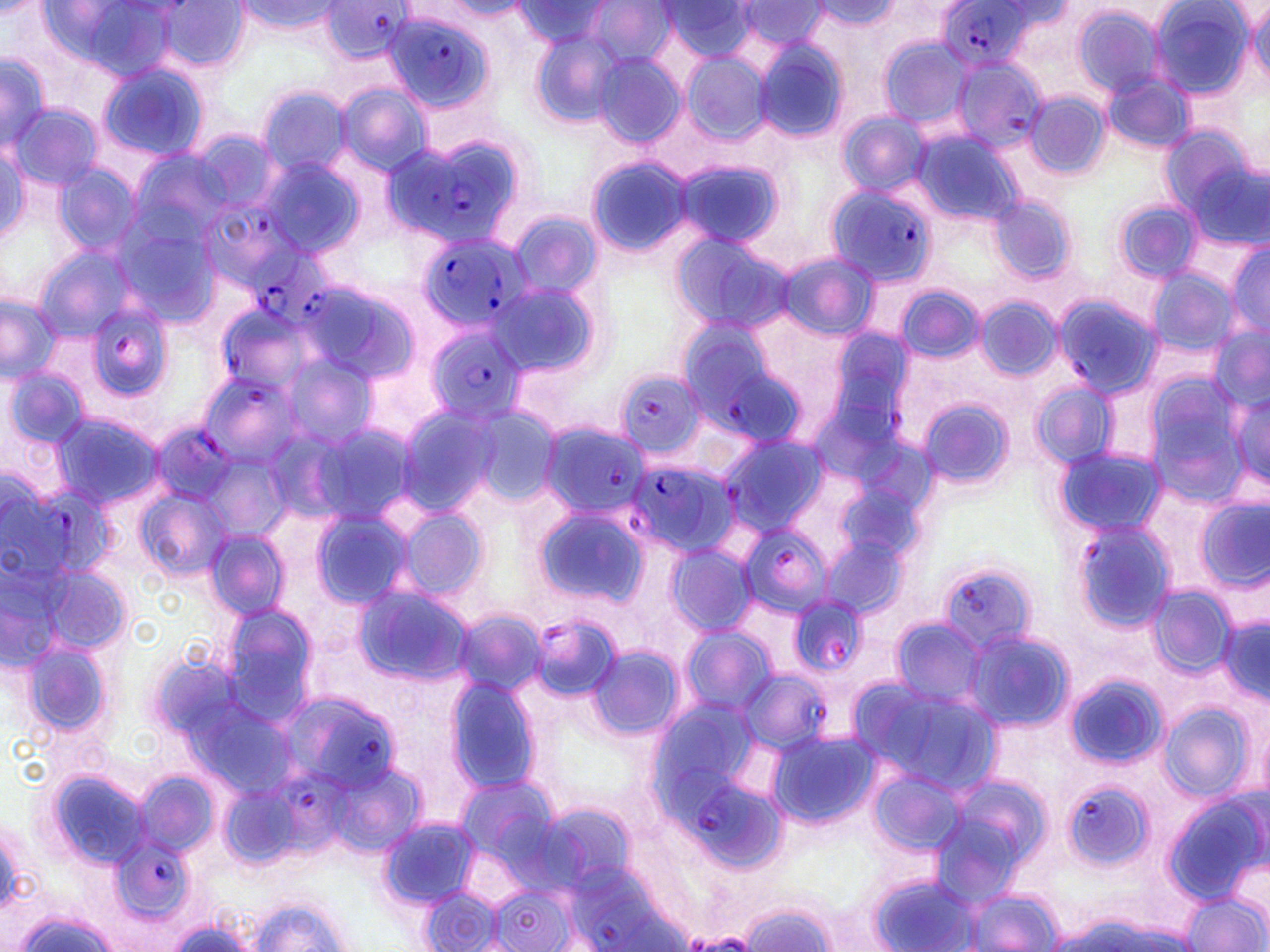
slide-level diagnosis = Plasmodium falciparum
stain = May-Grünwald-Giemsa
modality = optical microscopy
Plasmodium falciparum-infected red blood cell locations = approximate bounding boxes as (x1, y1, x2, y2) in pixels: (933, 1, 1053, 72), (377, 5, 498, 117), (948, 56, 1051, 154), (386, 130, 528, 249), (824, 182, 940, 287), (202, 204, 304, 291), (416, 229, 531, 336), (249, 242, 335, 324), (1052, 293, 1162, 399), (86, 298, 178, 403), (213, 301, 318, 398), (674, 313, 807, 445), (422, 322, 529, 426), (196, 369, 307, 469), (611, 369, 707, 459), (151, 422, 241, 503), (538, 422, 647, 519), (718, 436, 827, 535), (627, 458, 737, 561), (11, 477, 120, 585), (1072, 518, 1178, 634), (738, 523, 830, 620), (940, 565, 1041, 656), (787, 596, 869, 679), (739, 669, 830, 752), (287, 699, 398, 796), (669, 762, 754, 851), (267, 775, 361, 860), (1061, 779, 1153, 873), (108, 832, 194, 932)
image size = 1270×952 pixels
magnification = 1000x
field of view = one of a larger specimen
preparation = thin blood smear
uninfected red blood cell locations = approximate bounding boxes as (x1, y1, x2, y2) in pixels: (0, 0, 49, 17), (153, 1, 249, 74), (236, 1, 344, 37), (512, 1, 618, 48), (664, 1, 757, 62), (809, 1, 904, 33), (1147, 1, 1256, 100), (42, 2, 181, 82), (444, 2, 529, 19), (583, 2, 676, 66), (735, 2, 835, 51), (1246, 4, 1270, 82), (1070, 6, 1170, 98), (528, 30, 625, 129), (877, 37, 973, 129), (752, 38, 850, 144), (592, 51, 687, 146), (680, 52, 771, 146), (0, 56, 52, 150), (96, 62, 210, 163), (1103, 74, 1195, 154), (335, 82, 433, 175), (256, 86, 353, 177), (1024, 91, 1112, 180), (9, 104, 101, 192), (836, 111, 930, 198), (909, 125, 1023, 232), (0, 137, 30, 247), (1177, 141, 1267, 250), (128, 148, 231, 244), (257, 155, 369, 261), (586, 156, 696, 257), (672, 158, 786, 252), (52, 162, 145, 259), (989, 195, 1077, 285), (1113, 198, 1201, 284), (509, 211, 603, 302), (111, 213, 226, 331), (667, 230, 795, 332), (1226, 242, 1269, 340), (32, 245, 142, 343), (776, 252, 878, 340), (1145, 267, 1237, 357), (487, 276, 607, 383), (301, 278, 421, 390), (893, 283, 986, 365), (0, 292, 63, 383), (974, 296, 1062, 383), (1209, 324, 1270, 416), (271, 351, 379, 455), (4, 365, 90, 453), (1139, 373, 1254, 500), (1031, 382, 1118, 471), (1227, 388, 1269, 489), (917, 396, 1014, 492), (395, 402, 531, 519), (49, 411, 164, 512), (309, 419, 420, 528), (1056, 445, 1167, 538), (203, 454, 290, 539), (137, 486, 231, 583), (1194, 499, 1269, 591), (306, 504, 420, 612), (388, 504, 491, 605), (534, 504, 651, 612), (204, 529, 290, 622), (821, 536, 906, 619), (663, 542, 758, 639), (0, 549, 81, 675), (32, 560, 132, 662), (354, 584, 477, 688), (1147, 584, 1237, 679), (219, 602, 319, 719), (453, 608, 548, 701), (527, 610, 624, 705), (1216, 615, 1270, 699), (887, 618, 992, 712), (958, 625, 1074, 732), (679, 628, 777, 716), (15, 633, 120, 744), (585, 644, 684, 742), (1064, 672, 1170, 771), (444, 675, 542, 794), (853, 677, 1001, 800), (1158, 703, 1255, 802), (766, 729, 879, 830), (329, 759, 426, 859), (866, 767, 969, 858), (46, 768, 156, 872), (136, 770, 217, 861), (454, 773, 563, 872), (929, 776, 1052, 907), (1164, 792, 1267, 905), (0, 817, 36, 916), (377, 818, 480, 910), (865, 872, 983, 952), (484, 881, 587, 952), (418, 887, 507, 951), (961, 887, 1066, 951), (1182, 890, 1267, 952), (249, 896, 349, 951), (738, 902, 838, 952), (12, 909, 122, 952), (164, 917, 260, 952)